Classify this cell by malaria status.
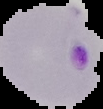
Parasitized.

image size = 103×109 pixels
preparation = thin blood smear
image type = segmented cell region on a black background